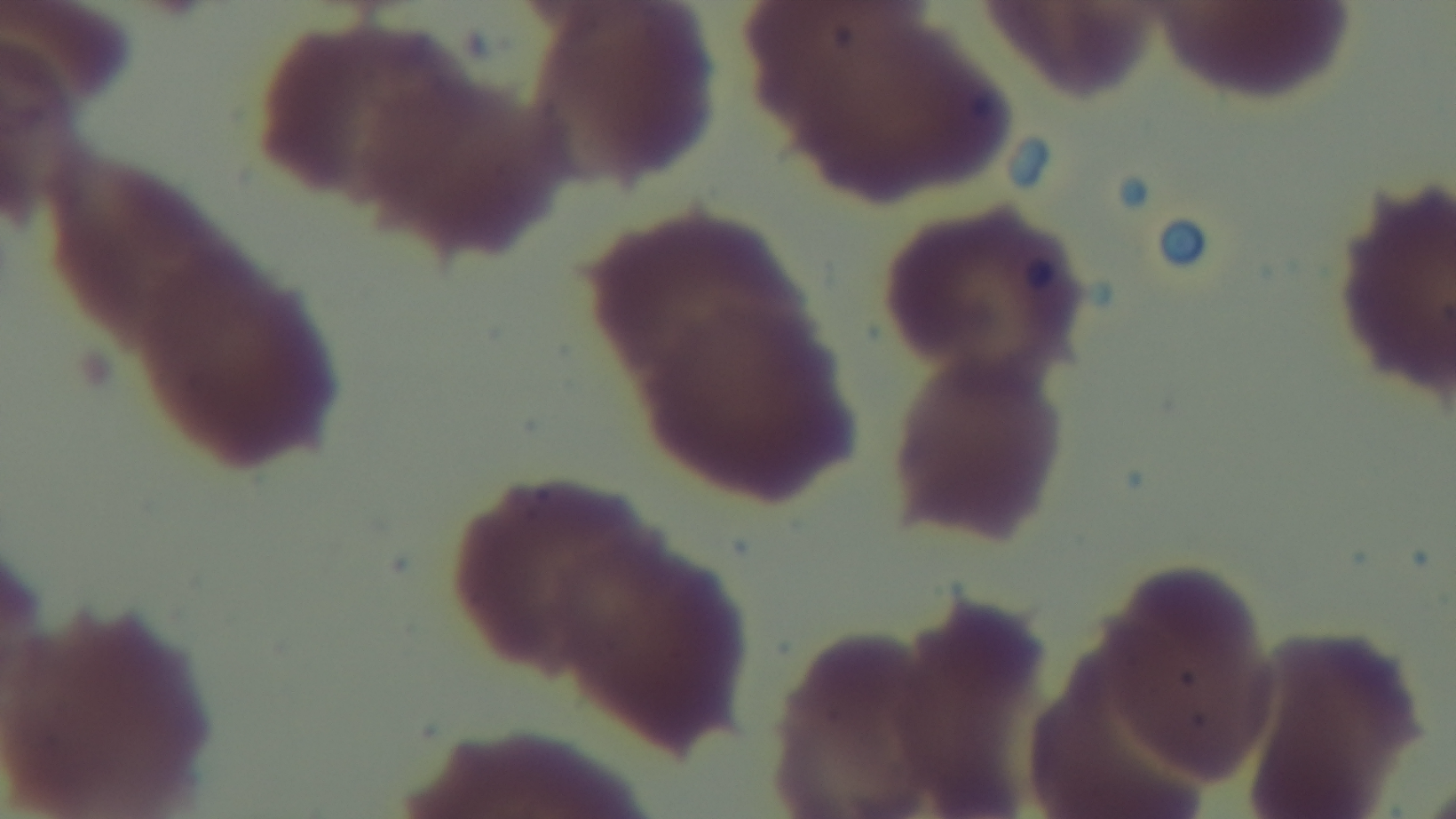
Summary:
  - Preparation: thin
  - Malaria status: negative
  - Modality: light microscopy
  - Field of view: one from the slide
  - Objective: 100x oil immersion
  - Capture: mounted 4K digital camera
  - Stain: Giemsa